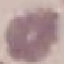
Summary:
  - Malaria status: uninfected
  - Stain: Giemsa
  - Capture: smartphone through the microscope eyepiece
  - Image type: cell patch, automatically extracted from a larger field of view and resized to 64 × 64 pixels
  - Preparation: thin smear